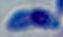

Summary:
  - Modality: micrograph
  - Magnification: 1000x
  - Identification: Toxoplasma gondii